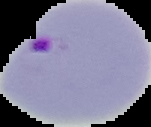

Summary:
  - Image type: cell region segmented out of the field of view; surrounding area masked to black
  - Image size: 151×127 pixels
  - Preparation: thin blood film
  - Result: malaria parasites identified